Outline each blood parasite and name the species.
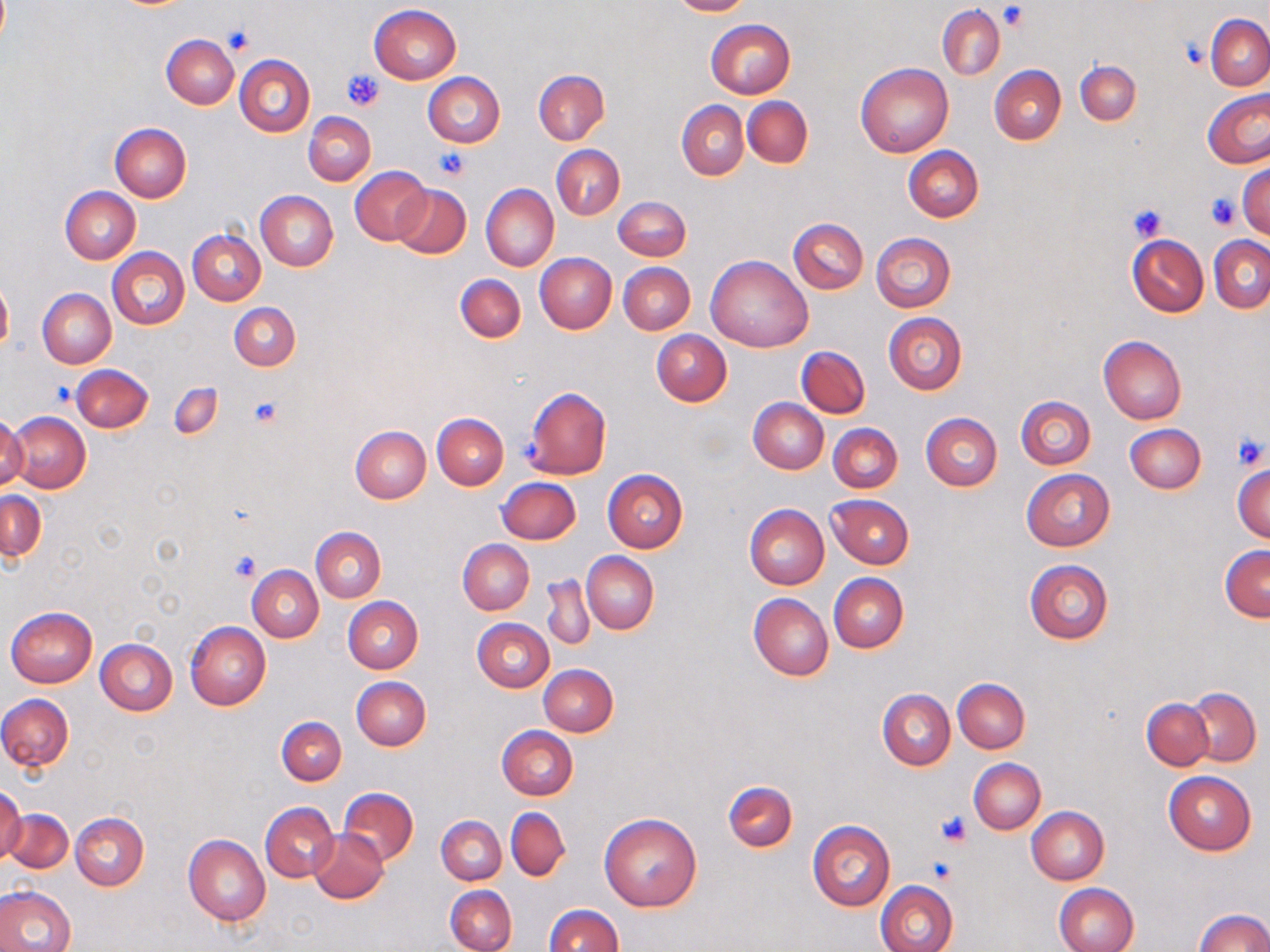

No blood parasites seen.

Summary:
  - Coordinate format: approximate bounding boxes as (x1, y1, x2, y2) in pixels
  - Platelet locations: (1000, 5, 1027, 30), (224, 24, 258, 55), (1183, 40, 1208, 68), (342, 68, 384, 111), (433, 148, 470, 180), (1206, 192, 1239, 228), (1129, 204, 1166, 242), (49, 382, 77, 408), (249, 395, 283, 427), (1232, 433, 1268, 471), (229, 552, 260, 582), (935, 810, 972, 847), (924, 857, 957, 885)
  - Uninfected red blood cell locations: (667, 0, 751, 17), (370, 4, 461, 84), (937, 5, 1004, 80), (1206, 15, 1270, 90), (706, 19, 796, 98), (161, 33, 240, 109), (235, 54, 315, 136), (1075, 60, 1140, 124), (856, 62, 954, 157), (989, 65, 1066, 145), (533, 70, 608, 144), (424, 72, 505, 148), (1202, 91, 1270, 168), (742, 96, 813, 168), (677, 100, 748, 180), (304, 112, 375, 185), (110, 123, 191, 203), (552, 145, 624, 219), (902, 145, 984, 222), (1238, 164, 1270, 239), (351, 166, 432, 245), (391, 183, 471, 258), (480, 183, 558, 272), (60, 186, 139, 264), (256, 191, 338, 271), (614, 196, 691, 261), (789, 218, 868, 293), (188, 229, 265, 305), (870, 233, 956, 312), (1127, 234, 1209, 317), (1209, 236, 1270, 313), (107, 248, 189, 330), (534, 253, 616, 333), (706, 254, 813, 352), (619, 262, 695, 335), (455, 274, 526, 343), (0, 278, 13, 354), (37, 289, 115, 368), (230, 302, 300, 371), (884, 312, 967, 394), (652, 330, 731, 406), (1098, 335, 1187, 423), (797, 345, 869, 417), (71, 364, 153, 432), (170, 383, 222, 440), (524, 387, 611, 479), (1016, 396, 1096, 469), (748, 398, 829, 474), (7, 412, 91, 493), (433, 412, 509, 489), (921, 412, 1003, 490), (0, 413, 27, 491), (828, 422, 902, 494), (1125, 423, 1205, 494), (350, 426, 431, 503), (1233, 463, 1270, 542), (603, 469, 689, 552), (1021, 469, 1115, 550), (496, 478, 580, 544), (1, 491, 47, 560), (826, 495, 914, 568), (744, 504, 829, 589), (311, 527, 385, 602), (458, 539, 535, 614), (1220, 544, 1270, 622), (582, 552, 658, 634), (1023, 559, 1113, 644), (247, 564, 322, 642), (829, 573, 908, 653), (543, 574, 595, 651), (748, 593, 832, 681), (344, 596, 423, 673), (6, 606, 97, 687), (473, 618, 554, 692), (184, 621, 271, 710), (95, 638, 177, 715), (538, 664, 618, 737), (351, 675, 431, 750), (953, 679, 1029, 753), (877, 688, 955, 770), (1186, 688, 1260, 766), (0, 695, 73, 771), (1143, 697, 1212, 769), (276, 717, 346, 785), (496, 726, 577, 801), (970, 758, 1045, 835), (1163, 772, 1256, 855), (722, 780, 797, 852), (0, 786, 26, 865), (338, 787, 418, 866), (260, 802, 339, 882), (505, 807, 571, 880), (1026, 807, 1108, 885), (4, 808, 72, 874), (599, 811, 703, 912), (69, 813, 148, 890), (436, 816, 506, 885), (807, 819, 896, 910), (308, 829, 388, 904), (183, 834, 271, 925), (876, 880, 957, 952), (1055, 882, 1139, 952), (0, 885, 75, 952), (445, 885, 516, 951), (543, 905, 622, 952), (1197, 909, 1270, 952)
  - Slide-level diagnosis: negative for blood parasites
  - Preparation: thin blood smear
  - Field of view: one of a larger specimen
  - Image size: 1270×952 pixels
  - Stain: May-Grünwald-Giemsa
  - Magnification: 1000x
  - Modality: light microscopy